Name the parasite shown.
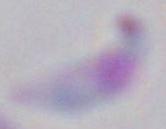
This is Toxoplasma gondii.

modality = micrograph
magnification = 1000x